Assess the morphology of the red blood cells.
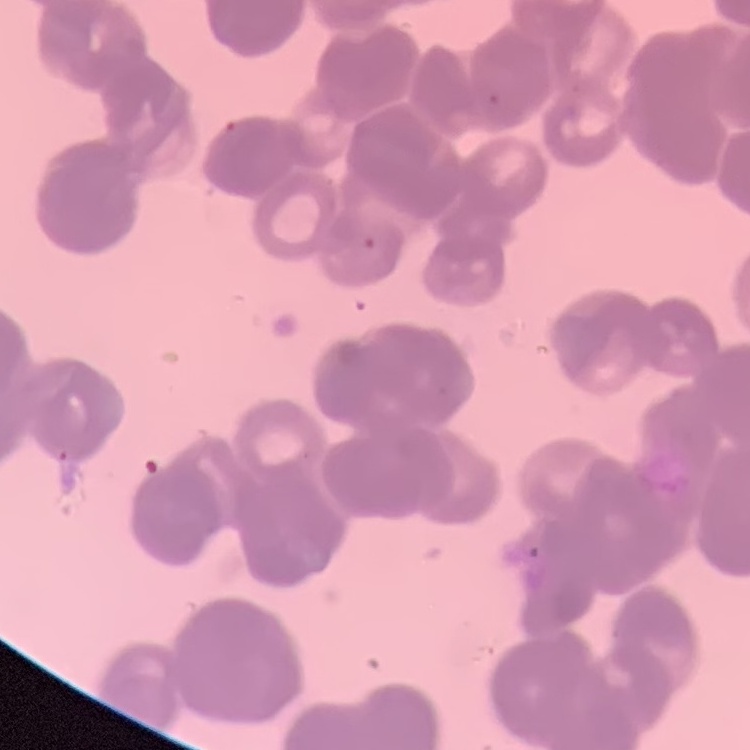
They show rouleaux formation.

image type = one tile cut from a larger photomicrograph
stain = Field's or Giemsa
preparation = thin peripheral smear